Outline each blood parasite and name the species.
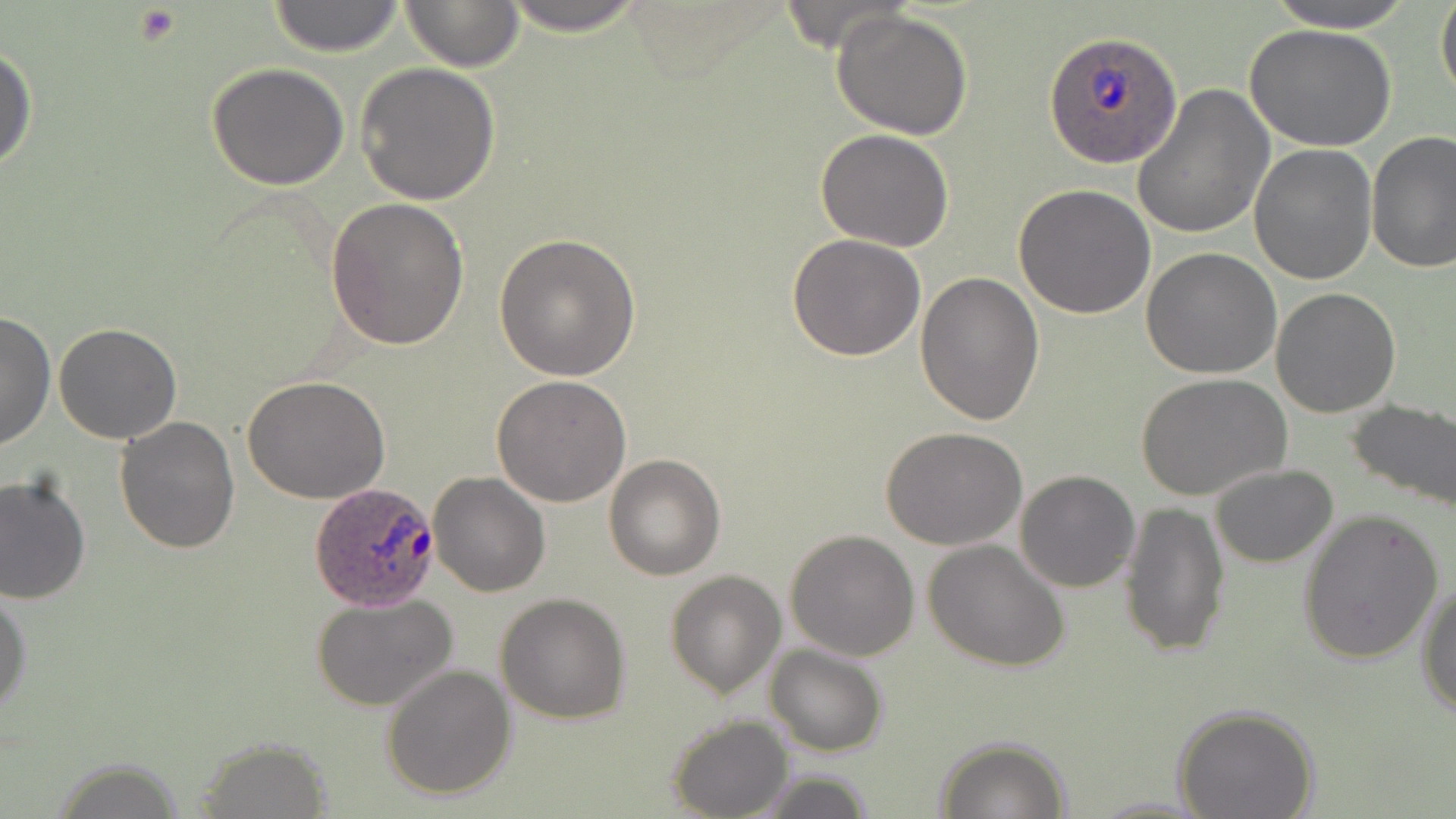

Approximate bounding boxes as named x1/y1/x2/y2 corners in pixels.
Plasmodium ovale-infected red blood cells: (x1=1044, y1=32, x2=1184, y2=169), (x1=309, y1=481, x2=441, y2=610).
No Plasmodium falciparum, Plasmodium malariae, Plasmodium vivax, Babesia divergens, or Trypanosoma brucei observed.

Uninfected red blood cell locations: (x1=264, y1=0, x2=408, y2=56), (x1=398, y1=0, x2=526, y2=71), (x1=490, y1=0, x2=656, y2=34), (x1=1257, y1=0, x2=1422, y2=32), (x1=1436, y1=0, x2=1456, y2=104), (x1=830, y1=8, x2=975, y2=139), (x1=1245, y1=24, x2=1396, y2=152), (x1=0, y1=43, x2=37, y2=176), (x1=355, y1=61, x2=500, y2=204), (x1=205, y1=63, x2=351, y2=189), (x1=1131, y1=85, x2=1275, y2=241), (x1=814, y1=127, x2=955, y2=252), (x1=1366, y1=131, x2=1456, y2=273), (x1=1249, y1=145, x2=1378, y2=285), (x1=1014, y1=184, x2=1156, y2=319), (x1=327, y1=197, x2=469, y2=348), (x1=495, y1=233, x2=641, y2=381), (x1=786, y1=234, x2=926, y2=360), (x1=1141, y1=248, x2=1282, y2=379), (x1=914, y1=269, x2=1043, y2=425), (x1=1270, y1=287, x2=1401, y2=417), (x1=0, y1=310, x2=55, y2=452), (x1=53, y1=323, x2=184, y2=444), (x1=1137, y1=374, x2=1292, y2=504), (x1=491, y1=375, x2=632, y2=506), (x1=243, y1=376, x2=390, y2=504), (x1=1345, y1=397, x2=1456, y2=514), (x1=114, y1=416, x2=241, y2=556), (x1=881, y1=426, x2=1028, y2=550), (x1=603, y1=453, x2=727, y2=580), (x1=1208, y1=463, x2=1339, y2=569), (x1=1015, y1=470, x2=1141, y2=593), (x1=428, y1=472, x2=550, y2=597), (x1=1, y1=473, x2=91, y2=607), (x1=1118, y1=500, x2=1230, y2=659), (x1=1296, y1=508, x2=1444, y2=663), (x1=786, y1=529, x2=920, y2=662), (x1=922, y1=539, x2=1070, y2=671), (x1=665, y1=569, x2=786, y2=698), (x1=1416, y1=580, x2=1456, y2=718), (x1=0, y1=588, x2=32, y2=720), (x1=312, y1=593, x2=458, y2=714), (x1=495, y1=593, x2=632, y2=723), (x1=764, y1=644, x2=888, y2=757), (x1=380, y1=663, x2=516, y2=800), (x1=1171, y1=702, x2=1320, y2=819), (x1=666, y1=714, x2=793, y2=819), (x1=933, y1=736, x2=1070, y2=818), (x1=191, y1=742, x2=333, y2=815), (x1=48, y1=759, x2=192, y2=818), (x1=749, y1=769, x2=877, y2=819), (x1=1086, y1=796, x2=1215, y2=817). Platelet locations: (x1=133, y1=5, x2=183, y2=45). Slide-level diagnosis: Plasmodium ovale. Thin blood smear. Single field of view. May-Grünwald-Giemsa-stained preparation. Optical microscopy. Image is 1456×819 pixels. 1000x magnification.